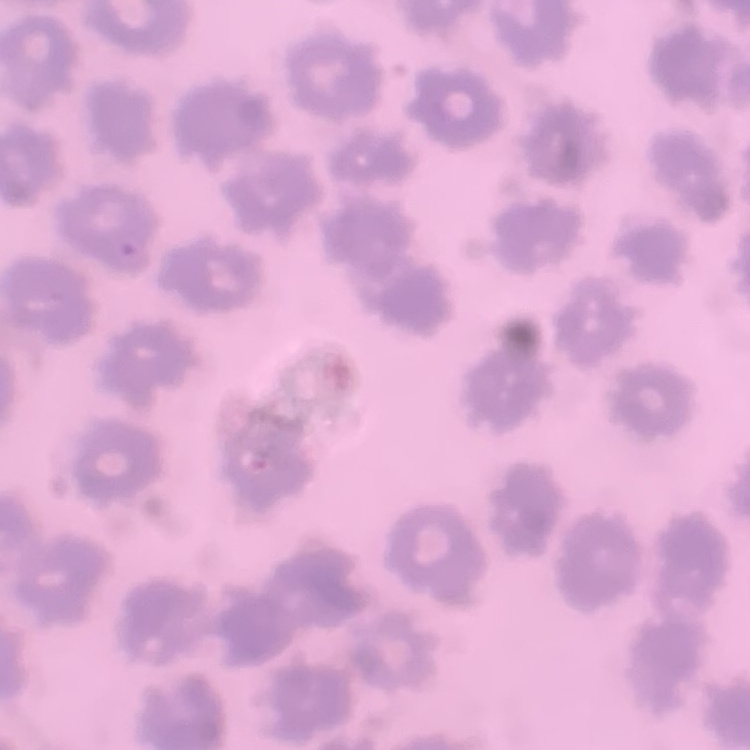

Summary:
  - Erythrocyte morphology: no rouleaux formation
  - Preparation: thin blood film
  - Image type: one tile cut from a larger photomicrograph
  - Stain: Field's or Giemsa